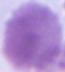
Summary:
  - Modality: photomicrograph
  - Identification: red blood cell
  - Magnification: 1000x